Point out each malaria parasite.
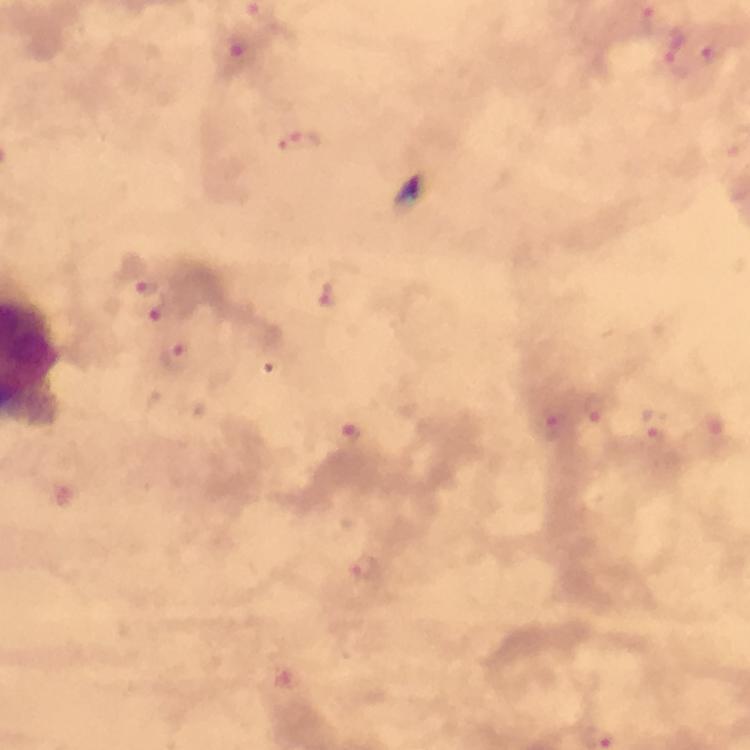

Approximate object centers, in pixels from the top-left corner.
Malaria parasites: (x=647, y=21), (x=712, y=50), (x=241, y=57), (x=679, y=57), (x=300, y=143), (x=148, y=290), (x=326, y=294), (x=165, y=315), (x=177, y=358), (x=595, y=409), (x=656, y=424), (x=550, y=430), (x=352, y=433), (x=366, y=569).

Photographed with a smartphone mounted on the microscope. Immersion oil applied. Thick blood film. Cropped region of a single field of view. From a diagnostic examination for malaria. Image is 750×750 pixels. At 100x magnification. Giemsa-stained preparation.